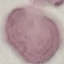
Result: negative for malaria parasites. Giemsa-stained preparation. Acquired by smartphone through the microscope eyepiece. Thin smear of blood. Cell patch, automatically extracted from a larger field of view and resized to 64 × 64 pixels.